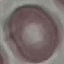
Summary:
  - Result: no malaria parasites seen
  - Capture: smartphone camera at the microscope eyepiece
  - Image type: automatically extracted cell patch, resized to 64 × 64 pixels
  - Stain: Giemsa
  - Preparation: thin blood smear